Comment on the morphology of the erythrocytes.
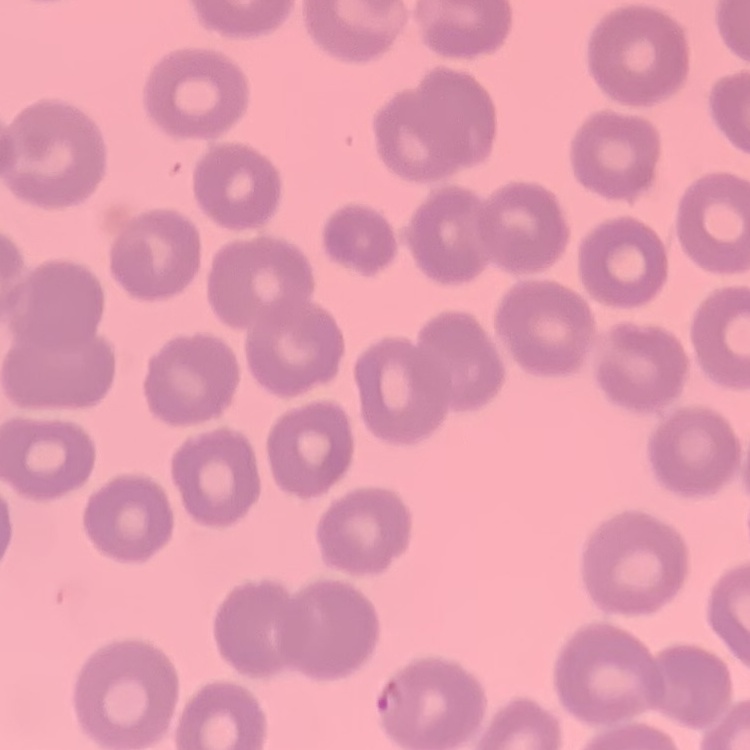
They show no rouleaux formation.

{
  "image_type": "square crop of a larger photomicrograph",
  "preparation": "thin blood film",
  "stain": "Field's or Giemsa"
}